Describe the morphology of the erythrocytes.
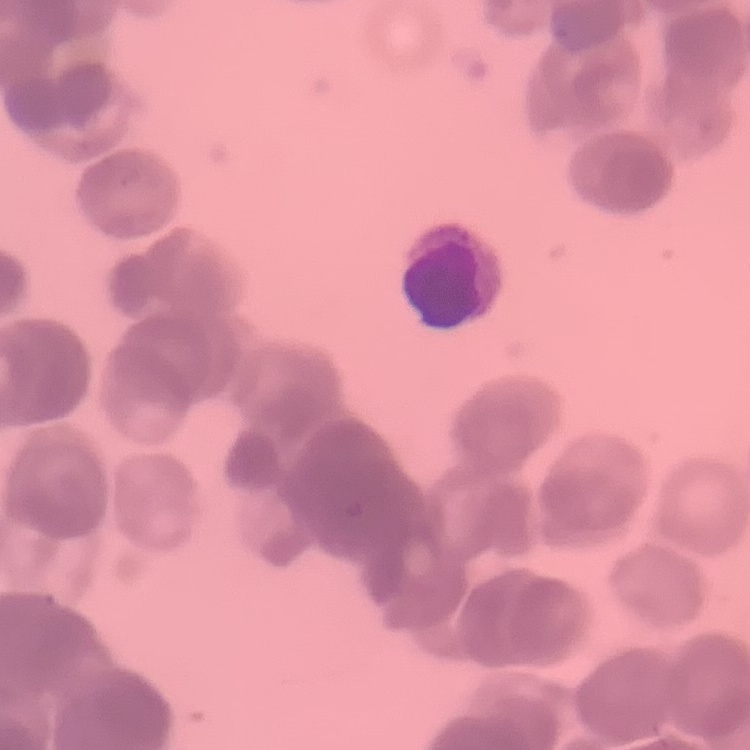

Rouleaux formation.

{
  "stain": "Field's or Giemsa",
  "image_type": "square crop of a larger photomicrograph",
  "preparation": "thin blood film"
}